Report the malaria status of this cell.
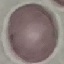

Uninfected.

Summary:
  - Stain: Giemsa
  - Preparation: thin blood smear
  - Image type: cell patch, automatically extracted from a larger field of view and resized to 64 × 64 pixels
  - Capture: smartphone camera at the microscope eyepiece